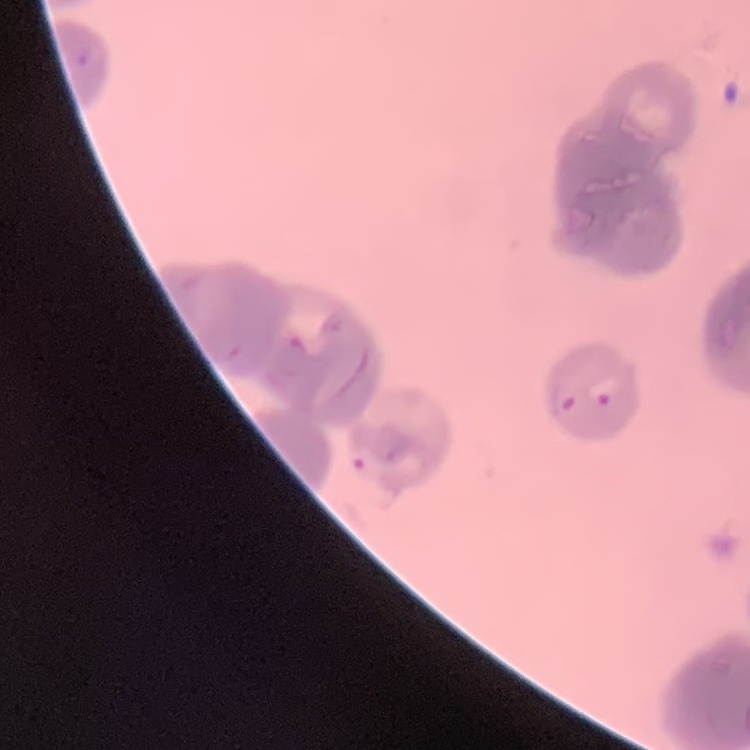

Summary:
  - Erythrocyte morphology: rouleaux formation
  - Stain: Field's or Giemsa
  - Image type: one tile cut from a larger photomicrograph
  - Preparation: thin blood film